Identify the preparation type.
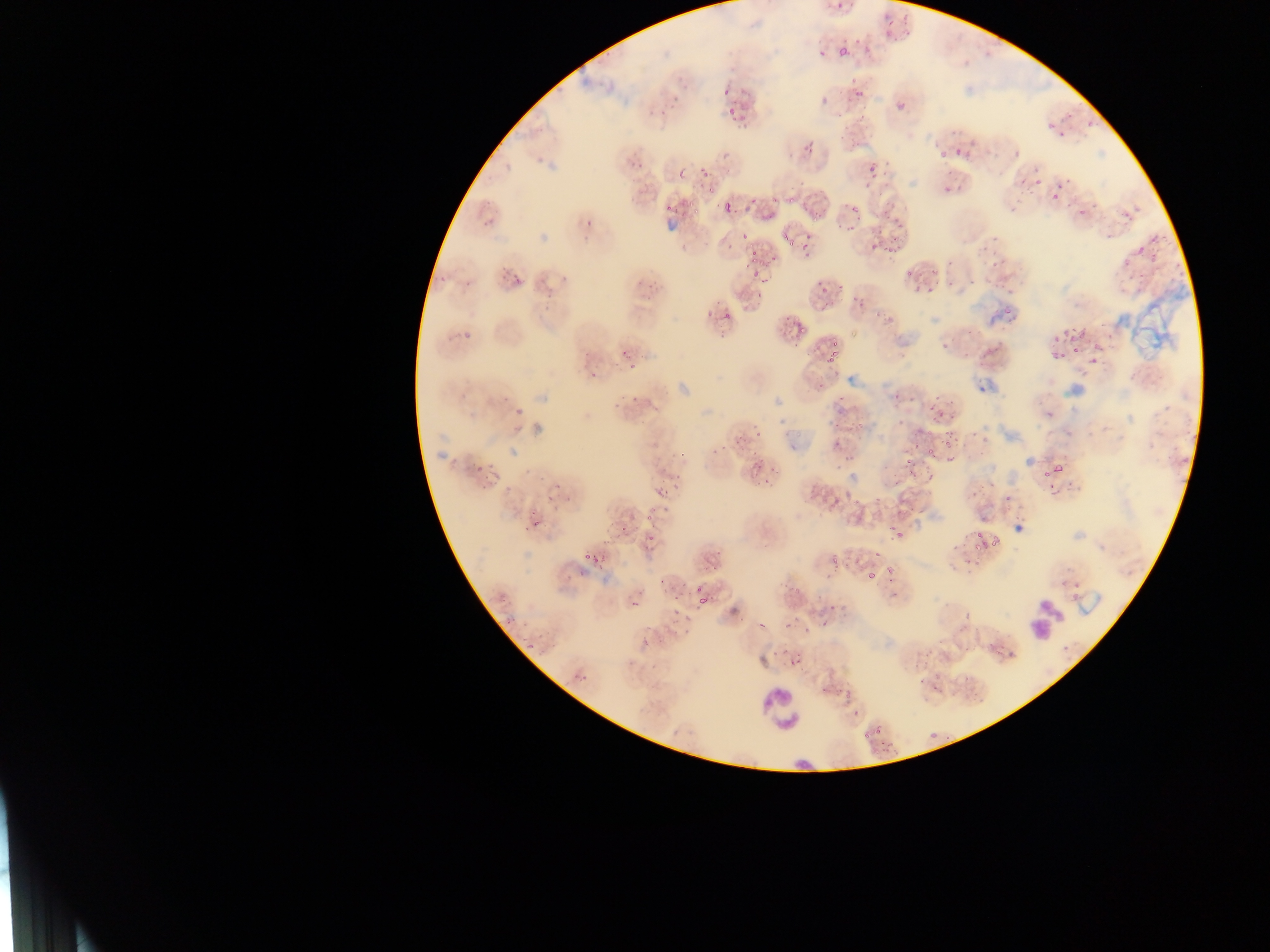

Thin blood film.

Approximate bounding boxes as [left, top, right, bottom] in pixels.
Summary:
  - Malaria parasite locations: [824, 0, 849, 14], [881, 12, 923, 40], [830, 25, 872, 56], [842, 84, 870, 102], [722, 87, 730, 97], [897, 103, 904, 111], [1042, 110, 1077, 127], [846, 119, 874, 147], [942, 138, 961, 154], [983, 143, 1003, 159], [695, 149, 733, 179], [865, 158, 886, 181], [1017, 167, 1039, 184], [634, 173, 665, 203], [941, 177, 965, 196], [1061, 181, 1103, 213], [1034, 185, 1048, 197], [1047, 190, 1060, 207], [1102, 198, 1149, 237], [838, 199, 868, 224], [688, 200, 702, 216], [712, 203, 743, 223], [758, 204, 782, 217], [666, 205, 675, 214], [790, 229, 813, 248], [1129, 231, 1164, 255], [742, 233, 766, 253], [864, 237, 894, 259], [978, 238, 993, 253], [498, 258, 531, 282], [749, 261, 782, 291], [1136, 261, 1150, 278], [982, 262, 1002, 273], [901, 265, 921, 280], [452, 267, 480, 291], [919, 280, 939, 294], [999, 288, 1008, 297], [720, 304, 735, 317], [452, 315, 479, 349], [764, 318, 802, 343], [1065, 330, 1082, 343], [817, 331, 856, 364], [926, 333, 953, 359], [974, 334, 1002, 354], [1076, 340, 1095, 352], [1047, 343, 1061, 357], [608, 354, 634, 372], [624, 375, 660, 406], [930, 402, 943, 419], [1099, 411, 1120, 428], [840, 423, 853, 440], [723, 431, 743, 448], [943, 431, 956, 442], [752, 435, 783, 463], [913, 438, 919, 447], [926, 448, 935, 461], [476, 452, 497, 480], [902, 459, 914, 476], [751, 465, 774, 486], [1048, 465, 1064, 474], [540, 474, 561, 485], [652, 476, 688, 527], [842, 494, 860, 508], [526, 498, 550, 528], [610, 507, 641, 546], [978, 522, 1001, 543], [893, 524, 905, 540], [582, 543, 599, 563], [861, 543, 893, 574], [836, 550, 850, 567], [951, 550, 972, 567], [663, 560, 683, 588], [1051, 577, 1083, 602], [685, 580, 727, 608], [626, 586, 647, 603], [499, 594, 528, 624], [786, 595, 820, 634], [669, 624, 680, 638], [990, 631, 1005, 640], [517, 635, 534, 652], [572, 652, 606, 680], [786, 654, 801, 664], [922, 664, 949, 692], [968, 674, 990, 691], [839, 690, 869, 710], [862, 742, 880, 758]
  - Leukocyte locations: [1024, 592, 1065, 645], [759, 688, 806, 733]
  - Field of view: single
  - Image size: 1270×952 pixels
  - Capture: mobile-phone photograph through a microscope
  - Country: Ghana